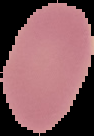

Summary:
  - Image type: cell region segmented out of the field of view; surrounding area masked to black
  - Result: negative for Plasmodium parasites
  - Preparation: thin blood film
  - Image size: 94×136 pixels